Identify the blood parasite species.
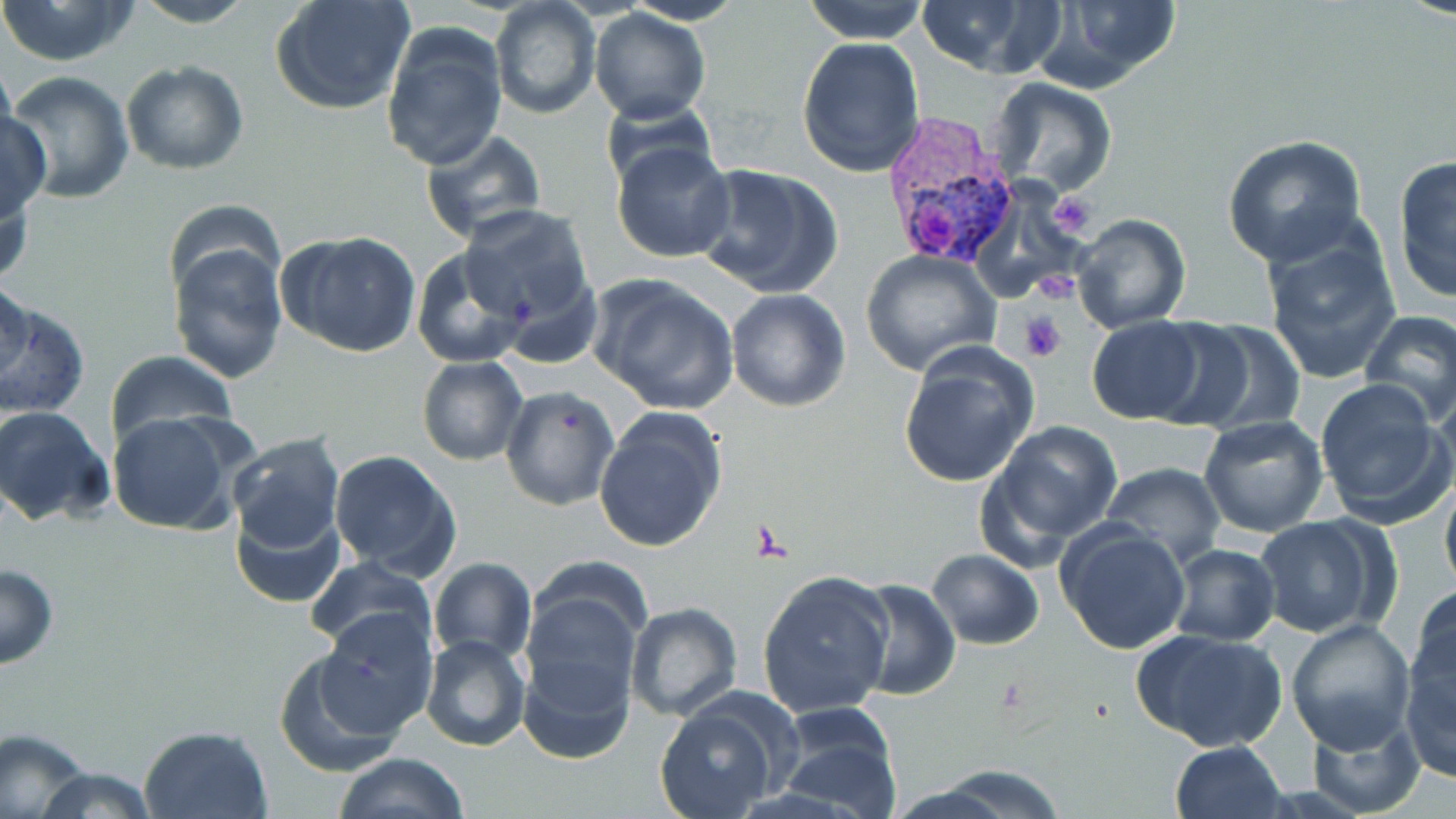
Plasmodium vivax.

{
  "stain": "May-Grünwald-Giemsa",
  "plasmodium_vivax_infected_red_blood_cell_locations": "approximate bounding boxes as named x1/y1/x2/y2 corners in pixels: (x1=874, y1=110, x2=1024, y2=267)",
  "preparation": "thin blood smear",
  "platelet_locations": "approximate bounding boxes as named x1/y1/x2/y2 corners in pixels: (x1=1046, y1=189, x2=1096, y2=237), (x1=1031, y1=271, x2=1077, y2=305), (x1=1020, y1=310, x2=1068, y2=361), (x1=749, y1=520, x2=789, y2=560)",
  "uninfected_red_blood_cell_locations": "approximate bounding boxes as named x1/y1/x2/y2 corners in pixels: (x1=0, y1=0, x2=143, y2=67), (x1=127, y1=0, x2=258, y2=27), (x1=269, y1=0, x2=417, y2=116), (x1=802, y1=0, x2=931, y2=44), (x1=913, y1=0, x2=1064, y2=78), (x1=1030, y1=0, x2=1183, y2=93), (x1=489, y1=2, x2=602, y2=120), (x1=588, y1=9, x2=712, y2=125), (x1=380, y1=22, x2=509, y2=172), (x1=797, y1=36, x2=926, y2=179), (x1=121, y1=59, x2=250, y2=175), (x1=5, y1=71, x2=135, y2=204), (x1=988, y1=78, x2=1118, y2=199), (x1=598, y1=95, x2=722, y2=193), (x1=0, y1=109, x2=50, y2=223), (x1=418, y1=128, x2=549, y2=244), (x1=1222, y1=134, x2=1367, y2=267), (x1=611, y1=141, x2=736, y2=264), (x1=1391, y1=153, x2=1456, y2=307), (x1=692, y1=163, x2=844, y2=299), (x1=1, y1=176, x2=35, y2=290), (x1=456, y1=205, x2=599, y2=334), (x1=1070, y1=212, x2=1192, y2=334), (x1=1259, y1=227, x2=1404, y2=387), (x1=277, y1=230, x2=423, y2=358), (x1=168, y1=239, x2=287, y2=382), (x1=410, y1=247, x2=530, y2=369), (x1=860, y1=250, x2=1001, y2=375), (x1=0, y1=273, x2=32, y2=388), (x1=592, y1=273, x2=739, y2=415), (x1=725, y1=289, x2=852, y2=411), (x1=0, y1=295, x2=90, y2=421), (x1=1359, y1=311, x2=1456, y2=427), (x1=1084, y1=316, x2=1211, y2=424), (x1=1166, y1=320, x2=1307, y2=436), (x1=897, y1=343, x2=1040, y2=492), (x1=103, y1=349, x2=236, y2=448), (x1=417, y1=358, x2=527, y2=464), (x1=1315, y1=378, x2=1449, y2=522), (x1=1431, y1=385, x2=1456, y2=509), (x1=501, y1=386, x2=619, y2=510), (x1=0, y1=404, x2=116, y2=528), (x1=592, y1=405, x2=728, y2=554), (x1=105, y1=411, x2=248, y2=536), (x1=1197, y1=415, x2=1328, y2=537), (x1=983, y1=419, x2=1124, y2=554), (x1=226, y1=431, x2=345, y2=563), (x1=328, y1=450, x2=462, y2=579), (x1=1100, y1=463, x2=1226, y2=567), (x1=1439, y1=473, x2=1456, y2=599), (x1=232, y1=501, x2=345, y2=610), (x1=1252, y1=516, x2=1386, y2=640), (x1=1054, y1=519, x2=1192, y2=655), (x1=1167, y1=544, x2=1280, y2=645), (x1=926, y1=548, x2=1045, y2=649), (x1=305, y1=556, x2=438, y2=661), (x1=428, y1=558, x2=537, y2=665), (x1=1, y1=563, x2=58, y2=671), (x1=756, y1=571, x2=895, y2=720), (x1=845, y1=578, x2=961, y2=701), (x1=521, y1=581, x2=645, y2=704), (x1=1408, y1=584, x2=1456, y2=703), (x1=625, y1=601, x2=742, y2=720), (x1=312, y1=607, x2=438, y2=739), (x1=1401, y1=608, x2=1456, y2=778), (x1=1285, y1=618, x2=1417, y2=755), (x1=1135, y1=630, x2=1285, y2=754), (x1=422, y1=635, x2=531, y2=752), (x1=273, y1=644, x2=413, y2=777), (x1=516, y1=650, x2=635, y2=764), (x1=652, y1=702, x2=781, y2=819), (x1=771, y1=704, x2=903, y2=819), (x1=1303, y1=710, x2=1423, y2=817), (x1=137, y1=724, x2=272, y2=819), (x1=1, y1=727, x2=94, y2=818), (x1=1169, y1=740, x2=1287, y2=819), (x1=332, y1=752, x2=471, y2=819), (x1=30, y1=762, x2=159, y2=819), (x1=925, y1=765, x2=1069, y2=818)",
  "magnification": "1000x",
  "image_size": "1456×819 pixels",
  "field_of_view": "one of a larger specimen",
  "modality": "light microscopy"
}